Locate every blood parasite and identify its species.
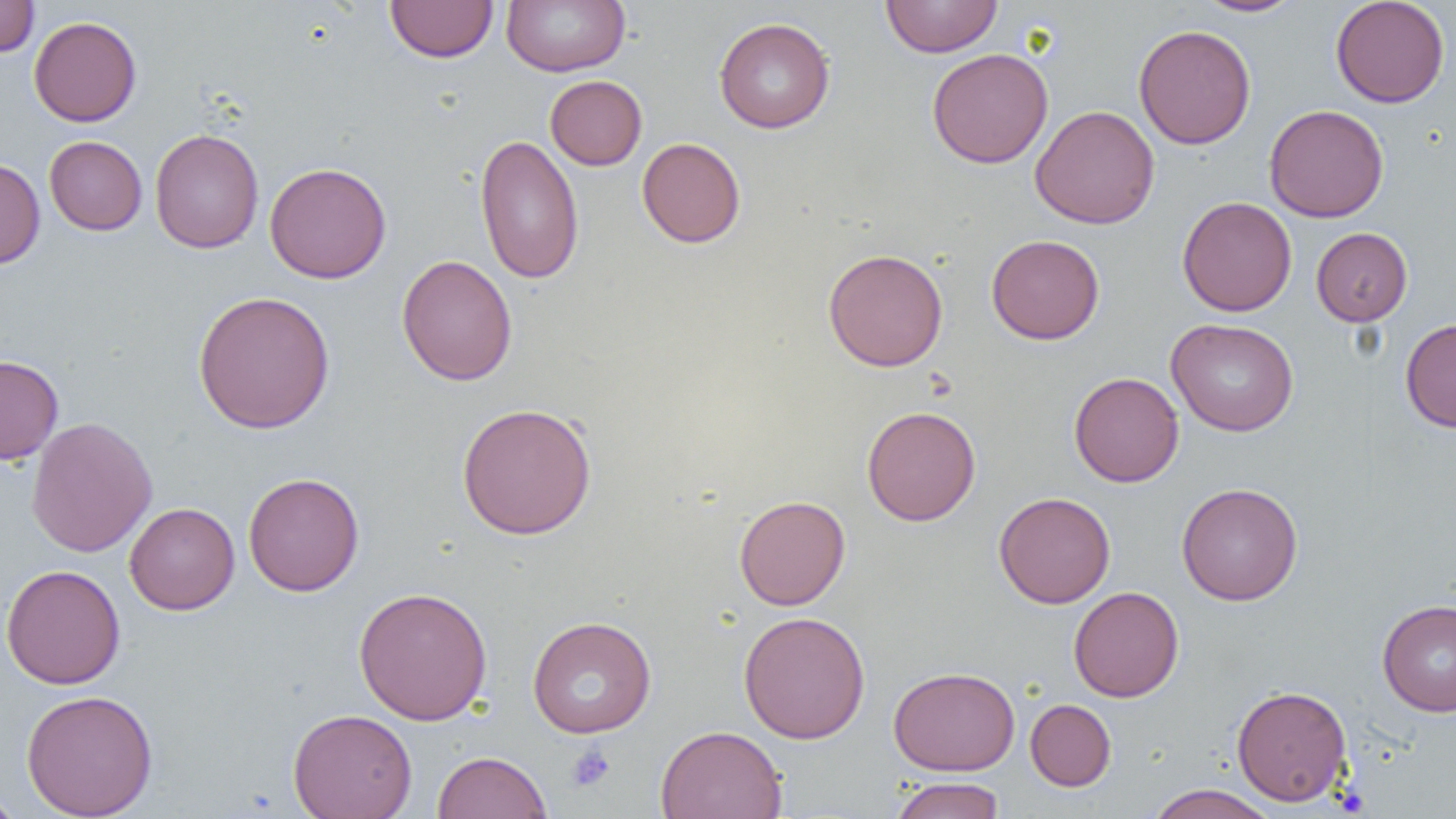
No blood parasites observed.

Approximate bounding boxes as (x1, y1, x2, y2) in pixels. Platelet locations: (566, 744, 615, 792). Uninfected red blood cell locations: (0, 0, 39, 58), (385, 0, 499, 63), (501, 0, 630, 76), (881, 0, 1002, 58), (1194, 0, 1305, 17), (1331, 0, 1450, 108), (29, 16, 142, 127), (714, 17, 835, 133), (1133, 24, 1256, 149), (926, 48, 1054, 168), (545, 75, 647, 170), (1264, 104, 1389, 223), (1030, 105, 1160, 229), (149, 128, 264, 253), (475, 133, 585, 284), (44, 135, 147, 235), (636, 137, 746, 248), (0, 158, 45, 270), (264, 162, 392, 284), (1177, 196, 1297, 316), (1311, 227, 1412, 326), (986, 234, 1105, 344), (822, 248, 948, 372), (396, 254, 517, 386), (193, 290, 336, 434), (1400, 317, 1456, 433), (1166, 318, 1299, 436), (0, 354, 64, 464), (1069, 371, 1184, 487), (456, 402, 597, 540), (861, 405, 981, 526), (26, 416, 157, 558), (243, 472, 365, 596), (1177, 482, 1303, 606), (994, 492, 1115, 609), (734, 495, 850, 610), (124, 502, 240, 615), (1, 564, 125, 690), (353, 586, 493, 726), (1068, 586, 1184, 702), (1377, 600, 1456, 716), (738, 611, 870, 744), (527, 615, 657, 738), (887, 665, 1021, 775), (1231, 684, 1352, 806), (21, 689, 158, 818), (1025, 699, 1116, 791), (288, 708, 417, 819), (656, 724, 787, 819), (432, 750, 552, 819), (889, 776, 1006, 819), (1146, 784, 1279, 819), (0, 787, 24, 819). Slide-level diagnosis: no evidence of blood parasites. Single field of view. Light microscopy. Captured at 1000x magnification. Image is 1456×819 pixels. Thin blood smear.